Name the parasite shown.
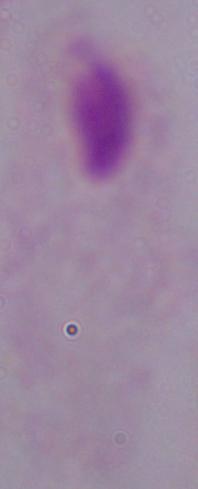

This is a trichomonad.

Summary:
  - Modality: micrograph
  - Magnification: 1000x